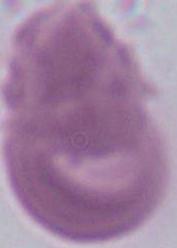 Photomicrograph. 1000x magnification. A red blood cell is seen.